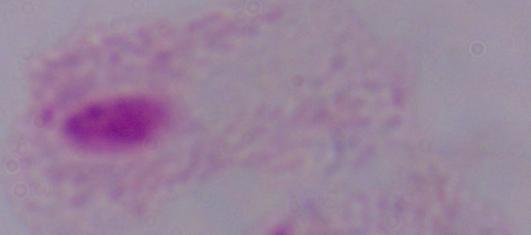

Summary:
  - Modality: photomicrograph
  - Magnification: 1000x
  - Identification: trichomonad